Evaluate for Plasmodium parasites.
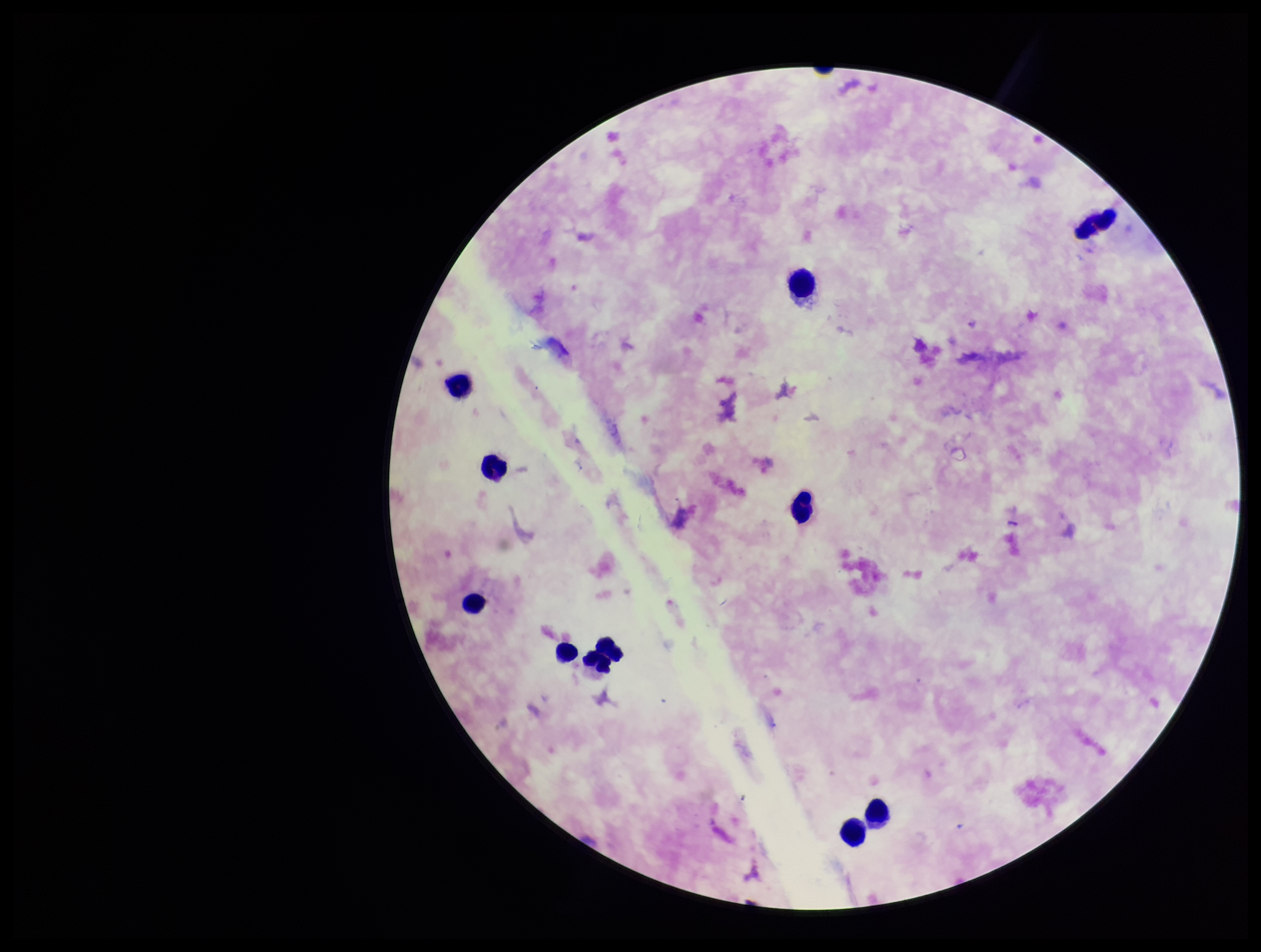
None seen.

Image is 1261×952 pixels. Parasite count: 0. Photographed through the microscope eyepiece with a smartphone camera. Leukocyte count: 11. One field from this slide. Preparation: thick. Species reported for this patient: Plasmodium falciparum. Stained with Giemsa. Patient malaria status: positive.